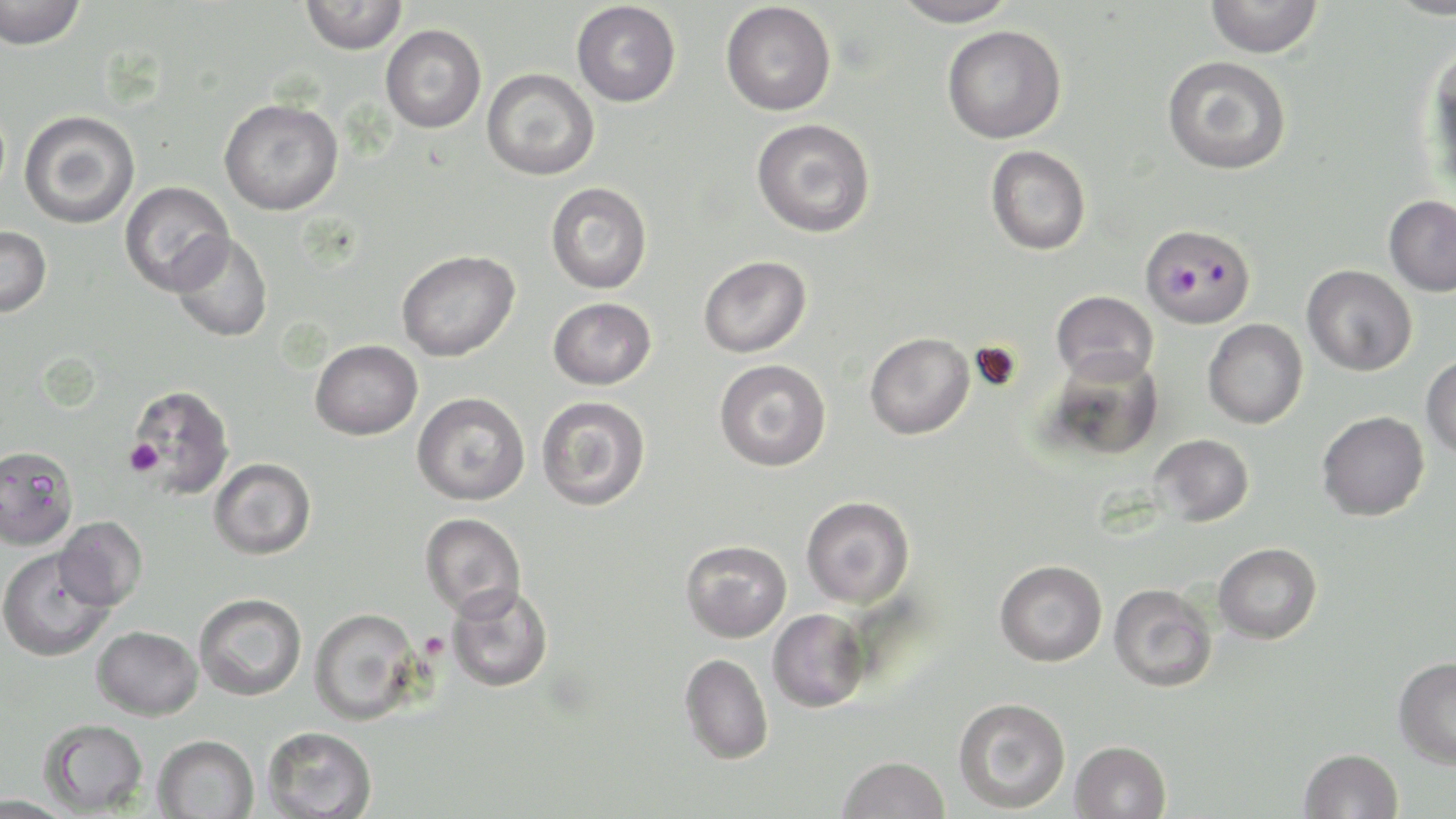
slide-level diagnosis = Plasmodium falciparum
modality = light microscopy
preparation = thin blood film
Plasmodium falciparum-infected red blood cell locations = approximate bounding boxes as named x1/y1/x2/y2 corners in pixels: (x1=1142, y1=225, x2=1254, y2=328)
platelet locations = approximate bounding boxes as named x1/y1/x2/y2 corners in pixels: (x1=125, y1=439, x2=163, y2=476)
image size = 1456×819 pixels
magnification = 1000x
stain = May-Grünwald-Giemsa
field of view = one of a larger specimen
uninfected red blood cell locations = approximate bounding boxes as named x1/y1/x2/y2 corners in pixels: (x1=0, y1=0, x2=87, y2=50), (x1=300, y1=0, x2=408, y2=54), (x1=888, y1=0, x2=1019, y2=28), (x1=1205, y1=0, x2=1324, y2=58), (x1=1385, y1=0, x2=1456, y2=19), (x1=572, y1=1, x2=681, y2=107), (x1=721, y1=2, x2=836, y2=116), (x1=380, y1=24, x2=486, y2=133), (x1=942, y1=25, x2=1067, y2=143), (x1=1422, y1=45, x2=1456, y2=186), (x1=1161, y1=55, x2=1292, y2=175), (x1=482, y1=68, x2=600, y2=180), (x1=219, y1=98, x2=344, y2=215), (x1=19, y1=110, x2=140, y2=229), (x1=751, y1=118, x2=876, y2=238), (x1=985, y1=145, x2=1091, y2=256), (x1=120, y1=181, x2=234, y2=296), (x1=545, y1=182, x2=652, y2=295), (x1=1383, y1=195, x2=1456, y2=296), (x1=0, y1=225, x2=52, y2=317), (x1=169, y1=232, x2=273, y2=343), (x1=397, y1=249, x2=519, y2=361), (x1=698, y1=255, x2=811, y2=358), (x1=1302, y1=264, x2=1417, y2=376), (x1=1051, y1=290, x2=1158, y2=384), (x1=548, y1=297, x2=656, y2=390), (x1=1203, y1=319, x2=1308, y2=429), (x1=865, y1=332, x2=975, y2=440), (x1=311, y1=339, x2=422, y2=440), (x1=1046, y1=349, x2=1164, y2=460), (x1=1421, y1=354, x2=1456, y2=459), (x1=714, y1=359, x2=831, y2=472), (x1=127, y1=385, x2=235, y2=498), (x1=412, y1=392, x2=530, y2=505), (x1=536, y1=396, x2=651, y2=511), (x1=1317, y1=411, x2=1430, y2=521), (x1=1150, y1=434, x2=1254, y2=526), (x1=0, y1=444, x2=80, y2=560), (x1=209, y1=457, x2=316, y2=560), (x1=801, y1=495, x2=915, y2=609), (x1=420, y1=513, x2=526, y2=619), (x1=55, y1=516, x2=147, y2=610), (x1=680, y1=540, x2=791, y2=642), (x1=1213, y1=542, x2=1321, y2=643), (x1=0, y1=548, x2=115, y2=661), (x1=994, y1=559, x2=1108, y2=666), (x1=446, y1=582, x2=554, y2=692), (x1=1108, y1=583, x2=1217, y2=692), (x1=194, y1=593, x2=307, y2=700), (x1=309, y1=607, x2=421, y2=725), (x1=767, y1=609, x2=870, y2=713), (x1=92, y1=626, x2=202, y2=720), (x1=679, y1=653, x2=774, y2=764), (x1=1393, y1=656, x2=1456, y2=768), (x1=953, y1=697, x2=1071, y2=813), (x1=39, y1=719, x2=148, y2=815), (x1=262, y1=726, x2=377, y2=818), (x1=153, y1=734, x2=259, y2=819), (x1=1070, y1=740, x2=1172, y2=819), (x1=1299, y1=748, x2=1403, y2=819), (x1=837, y1=755, x2=950, y2=818), (x1=1, y1=795, x2=76, y2=819)